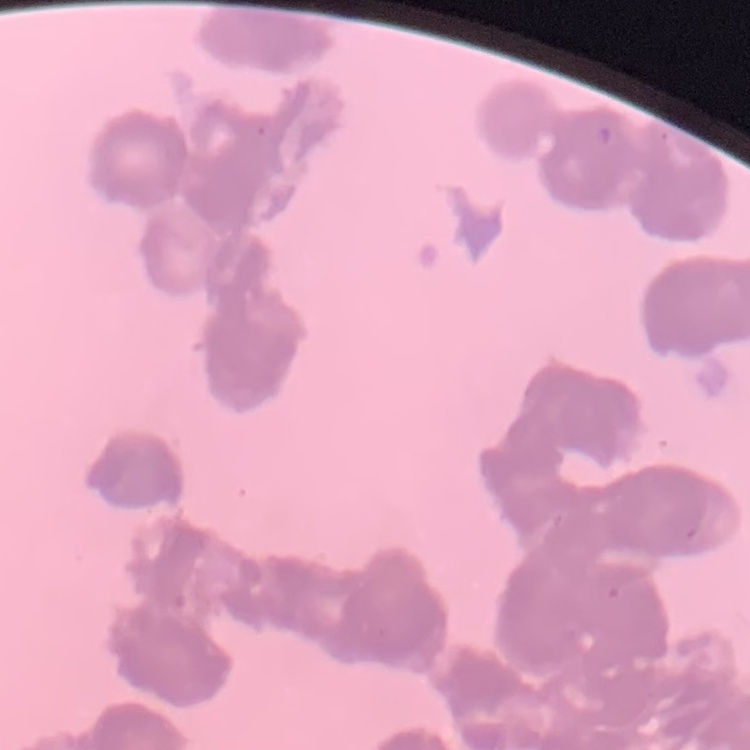 The red blood cells exhibit rouleaux formation. Field's or Giemsa stain. One tile cut from a larger photomicrograph. Thin blood film.